Describe the morphology of the red blood cells.
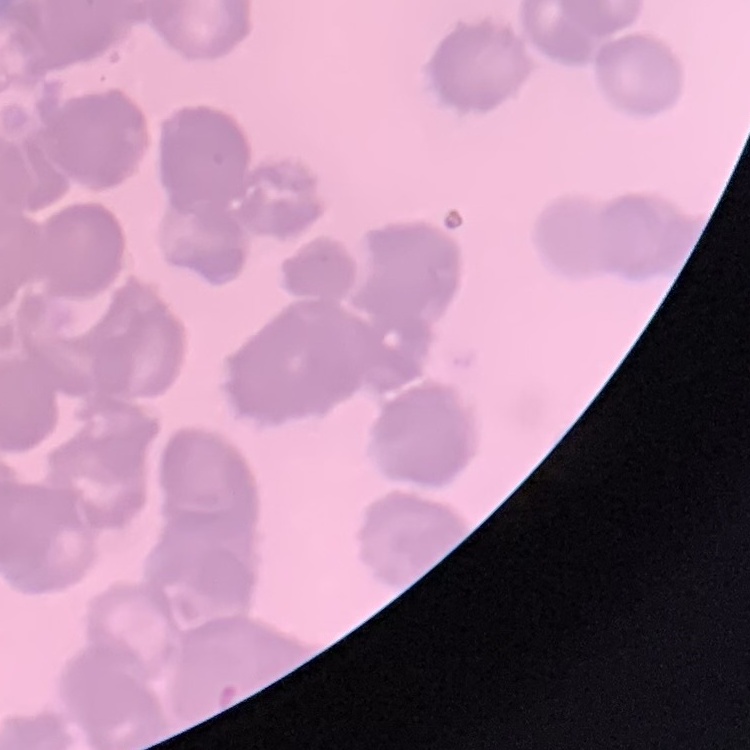

Rouleaux formation.

image_type: square crop of a larger photomicrograph
preparation: thin blood smear
stain: Field's or Giemsa